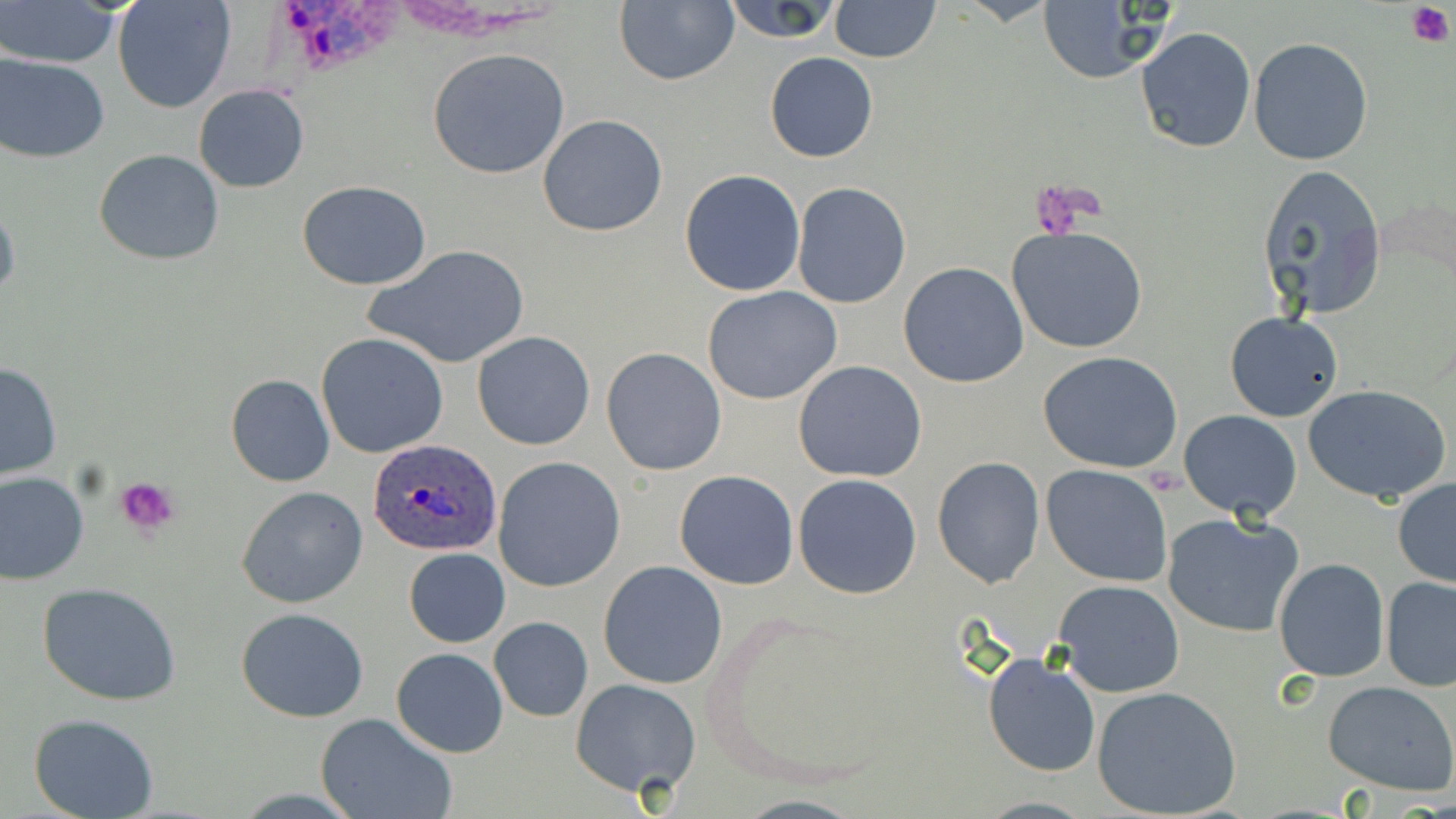
Summary:
  - Coordinate format: approximate bounding boxes as (x1,y1)-(x2,y2) corner pairs in pixels
  - Uninfected red blood cell locations: (718,0)-(847,43), (5,1)-(121,68), (111,1)-(237,114), (828,1)-(942,62), (612,2)-(740,86), (1033,4)-(1165,82), (1136,27)-(1256,152), (1248,37)-(1373,166), (426,48)-(571,179), (1,51)-(109,162), (765,51)-(878,163), (193,85)-(310,193), (537,113)-(668,238), (94,150)-(224,264), (1256,163)-(1386,321), (679,169)-(806,297), (297,180)-(434,290), (791,183)-(911,308), (0,197)-(20,311), (1008,227)-(1150,353), (367,243)-(529,370), (898,262)-(1029,388), (702,287)-(844,404), (1225,312)-(1343,422), (472,331)-(596,450), (316,333)-(450,460), (600,347)-(727,477), (1037,350)-(1183,473), (0,361)-(63,481), (793,361)-(928,482), (225,373)-(335,487), (1303,384)-(1453,505), (1179,410)-(1301,522), (493,456)-(626,592), (932,457)-(1045,588), (1040,464)-(1173,587), (0,470)-(89,585), (674,470)-(799,590), (794,474)-(923,599), (1392,476)-(1456,588), (237,486)-(368,608), (1162,513)-(1305,639), (403,547)-(510,647), (1273,558)-(1391,683), (598,561)-(728,688), (1381,577)-(1456,691), (1053,580)-(1185,697), (36,581)-(182,705), (235,607)-(368,722), (489,618)-(593,721), (392,647)-(507,756), (981,651)-(1101,778), (571,678)-(699,797), (1323,680)-(1456,795), (1092,685)-(1243,818), (29,713)-(160,819), (317,713)-(457,819), (973,795)-(1097,817)
  - Platelet locations: (1404,3)-(1454,48), (115,476)-(179,536)
  - Plasmodium ovale-infected red blood cell locations: (367,438)-(503,557)
  - Slide-level diagnosis: Plasmodium ovale
  - Image size: 1456×819 pixels
  - Stain: May-Grünwald-Giemsa
  - Magnification: 1000x
  - Modality: light microscopy
  - Preparation: thin blood film
  - Field of view: single